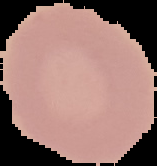

From a thin blood smear. Image is 157×166 pixels. Malaria status: uninfected. Cell region segmented out of the field of view; the surrounding area is masked to black.